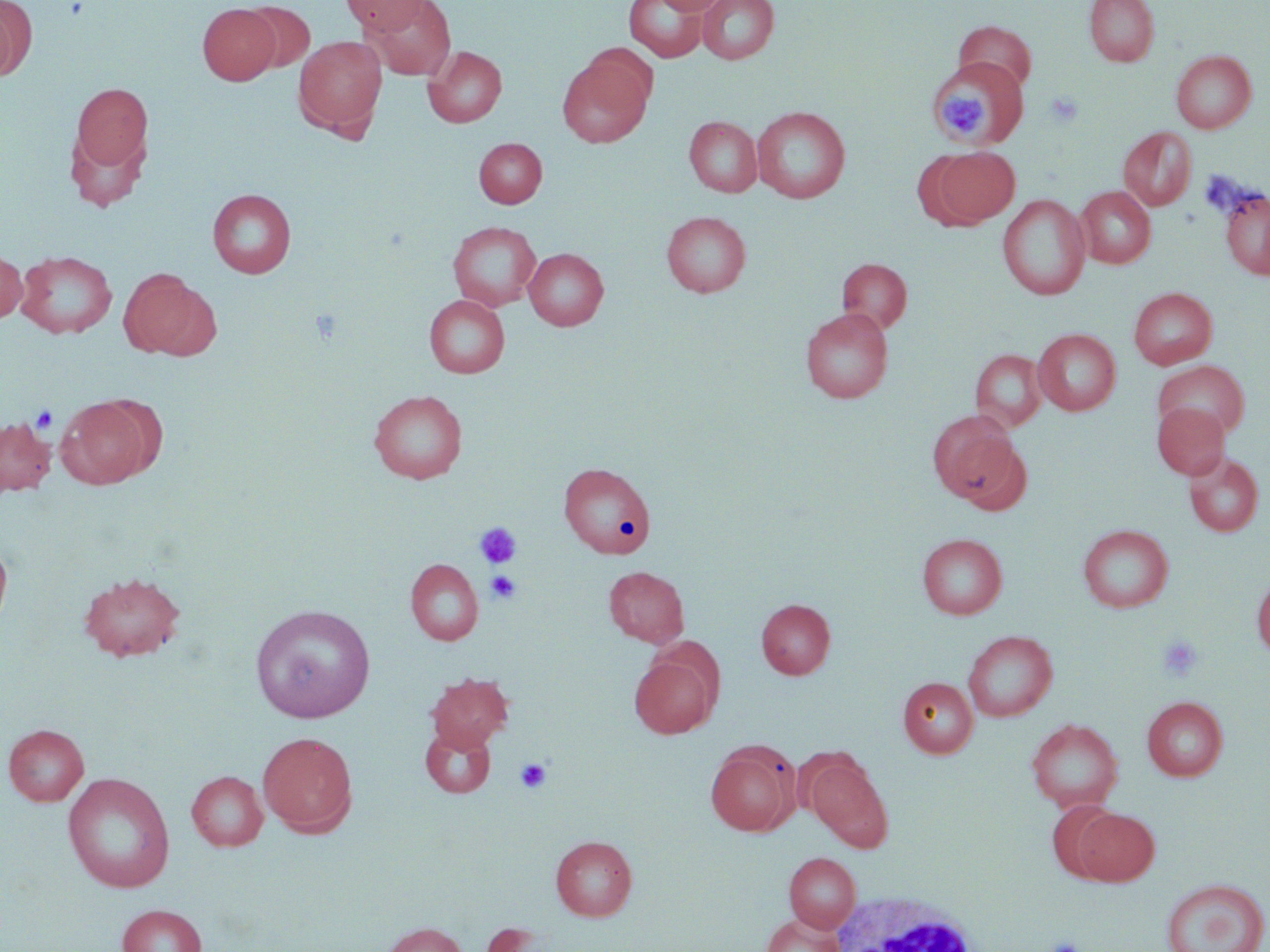
slide-level diagnosis = negative for blood parasites
uninfected red blood cell locations = approximate bounding boxes as named x1/y1/x2/y2 corners in pixels: (x1=0, y1=0, x2=36, y2=81), (x1=343, y1=0, x2=430, y2=34), (x1=366, y1=0, x2=455, y2=80), (x1=624, y1=0, x2=708, y2=62), (x1=652, y1=0, x2=730, y2=15), (x1=698, y1=0, x2=779, y2=64), (x1=1083, y1=0, x2=1159, y2=66), (x1=241, y1=1, x2=316, y2=74), (x1=197, y1=4, x2=280, y2=85), (x1=953, y1=20, x2=1036, y2=93), (x1=293, y1=35, x2=387, y2=136), (x1=423, y1=45, x2=507, y2=127), (x1=1171, y1=50, x2=1256, y2=133), (x1=557, y1=55, x2=652, y2=147), (x1=929, y1=59, x2=1028, y2=149), (x1=69, y1=81, x2=154, y2=184), (x1=751, y1=106, x2=851, y2=203), (x1=684, y1=116, x2=762, y2=197), (x1=1118, y1=127, x2=1196, y2=210), (x1=474, y1=138, x2=547, y2=208), (x1=925, y1=146, x2=1020, y2=229), (x1=1076, y1=186, x2=1156, y2=268), (x1=1218, y1=187, x2=1270, y2=280), (x1=207, y1=189, x2=296, y2=278), (x1=997, y1=194, x2=1090, y2=300), (x1=661, y1=211, x2=751, y2=297), (x1=448, y1=221, x2=542, y2=310), (x1=0, y1=248, x2=27, y2=323), (x1=523, y1=248, x2=608, y2=330), (x1=16, y1=250, x2=117, y2=338), (x1=837, y1=257, x2=912, y2=333), (x1=118, y1=268, x2=217, y2=360), (x1=1129, y1=287, x2=1218, y2=369), (x1=424, y1=295, x2=509, y2=378), (x1=800, y1=308, x2=893, y2=403), (x1=1033, y1=328, x2=1121, y2=415), (x1=970, y1=349, x2=1047, y2=432), (x1=1154, y1=360, x2=1250, y2=442), (x1=368, y1=389, x2=467, y2=483), (x1=56, y1=396, x2=156, y2=489), (x1=1152, y1=403, x2=1230, y2=479), (x1=930, y1=415, x2=1026, y2=508), (x1=0, y1=417, x2=56, y2=496), (x1=1183, y1=451, x2=1265, y2=537), (x1=558, y1=462, x2=656, y2=558), (x1=1078, y1=524, x2=1173, y2=612), (x1=916, y1=533, x2=1007, y2=619), (x1=0, y1=536, x2=13, y2=636), (x1=405, y1=559, x2=483, y2=644), (x1=603, y1=566, x2=689, y2=647), (x1=78, y1=572, x2=186, y2=662), (x1=1251, y1=573, x2=1270, y2=660), (x1=756, y1=599, x2=836, y2=679), (x1=250, y1=604, x2=375, y2=723), (x1=963, y1=630, x2=1057, y2=722), (x1=629, y1=652, x2=719, y2=739), (x1=426, y1=672, x2=514, y2=751), (x1=898, y1=677, x2=978, y2=757), (x1=1142, y1=696, x2=1228, y2=781), (x1=1026, y1=718, x2=1124, y2=812), (x1=3, y1=724, x2=89, y2=806), (x1=420, y1=725, x2=496, y2=798), (x1=258, y1=731, x2=358, y2=836), (x1=705, y1=744, x2=798, y2=836), (x1=806, y1=755, x2=893, y2=850), (x1=187, y1=771, x2=268, y2=851), (x1=62, y1=773, x2=175, y2=893), (x1=1047, y1=801, x2=1121, y2=880), (x1=1073, y1=808, x2=1159, y2=885), (x1=550, y1=835, x2=637, y2=921), (x1=784, y1=852, x2=860, y2=933), (x1=1160, y1=878, x2=1268, y2=952), (x1=117, y1=904, x2=208, y2=952), (x1=762, y1=914, x2=843, y2=952), (x1=378, y1=921, x2=467, y2=952), (x1=478, y1=922, x2=548, y2=952)
magnification = 1000x
white blood cell locations = approximate bounding boxes as named x1/y1/x2/y2 corners in pixels: (x1=827, y1=891, x2=979, y2=952)
platelet locations = approximate bounding boxes as named x1/y1/x2/y2 corners in pixels: (x1=941, y1=86, x2=993, y2=132), (x1=1044, y1=91, x2=1084, y2=127), (x1=308, y1=310, x2=345, y2=345), (x1=31, y1=405, x2=58, y2=434), (x1=474, y1=522, x2=522, y2=569), (x1=485, y1=570, x2=522, y2=604), (x1=1157, y1=635, x2=1204, y2=682), (x1=515, y1=757, x2=552, y2=793), (x1=1044, y1=936, x2=1085, y2=952)
field of view = single
stain = May-Grünwald-Giemsa
preparation = thin blood smear
image size = 1270×952 pixels
modality = optical microscopy